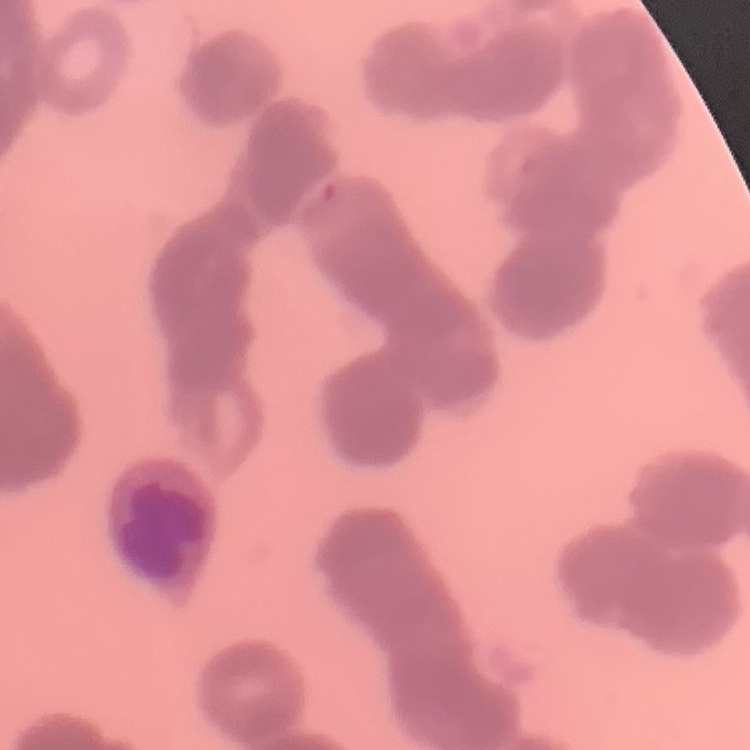
The erythrocytes exhibit rouleaux formation. Stained with either Field's or Giemsa. Square crop of a larger photomicrograph. Thin blood film.